Identify the parasite.
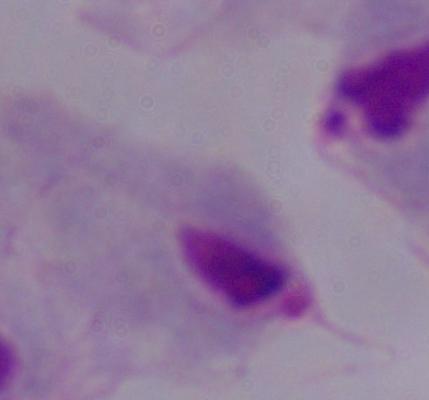
A trichomonad.

modality = photomicrograph
magnification = 1000x